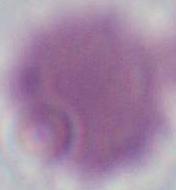

magnification = 1000x
modality = photomicrograph
identification = erythrocyte